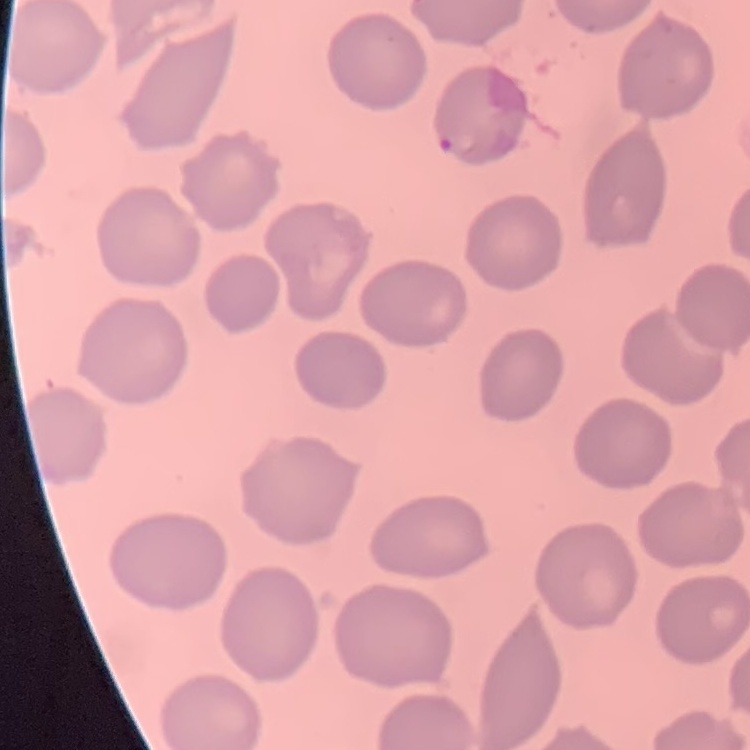

erythrocyte morphology = no rouleaux formation
preparation = thin blood film
image type = square crop of a larger photomicrograph
stain = Field's or Giemsa